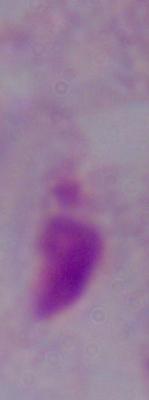
1000x magnification. Micrograph. A trichomonad is seen.